Describe the morphology of the red blood cells.
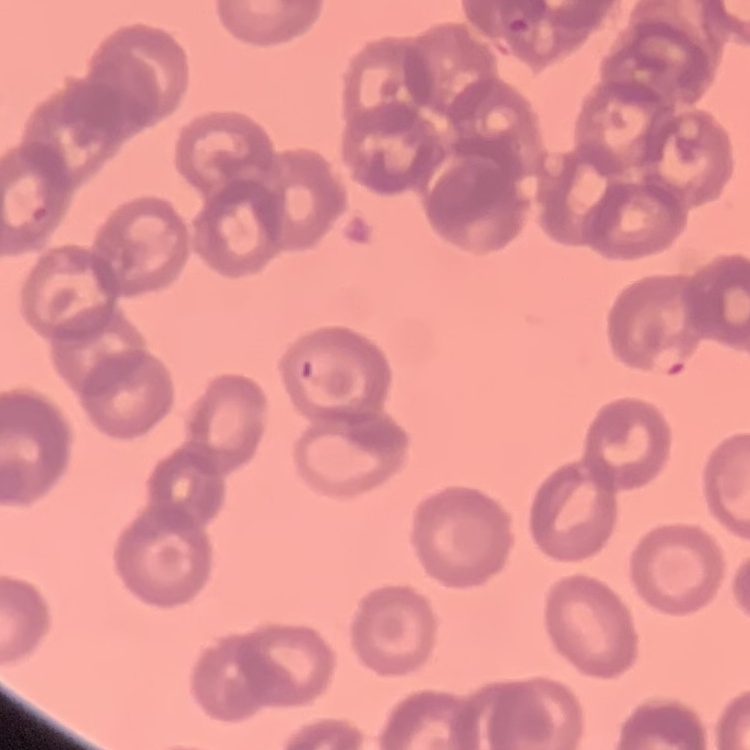

They show rouleaux formation.

Summary:
  - Stain: Field's or Giemsa
  - Image type: square crop of a larger photomicrograph
  - Preparation: thin blood smear